Report the malaria status of this cell.
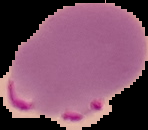
Parasitized.

The area outside the segmented cell region is set to black. Image is 148×130 pixels. From a thin blood film.